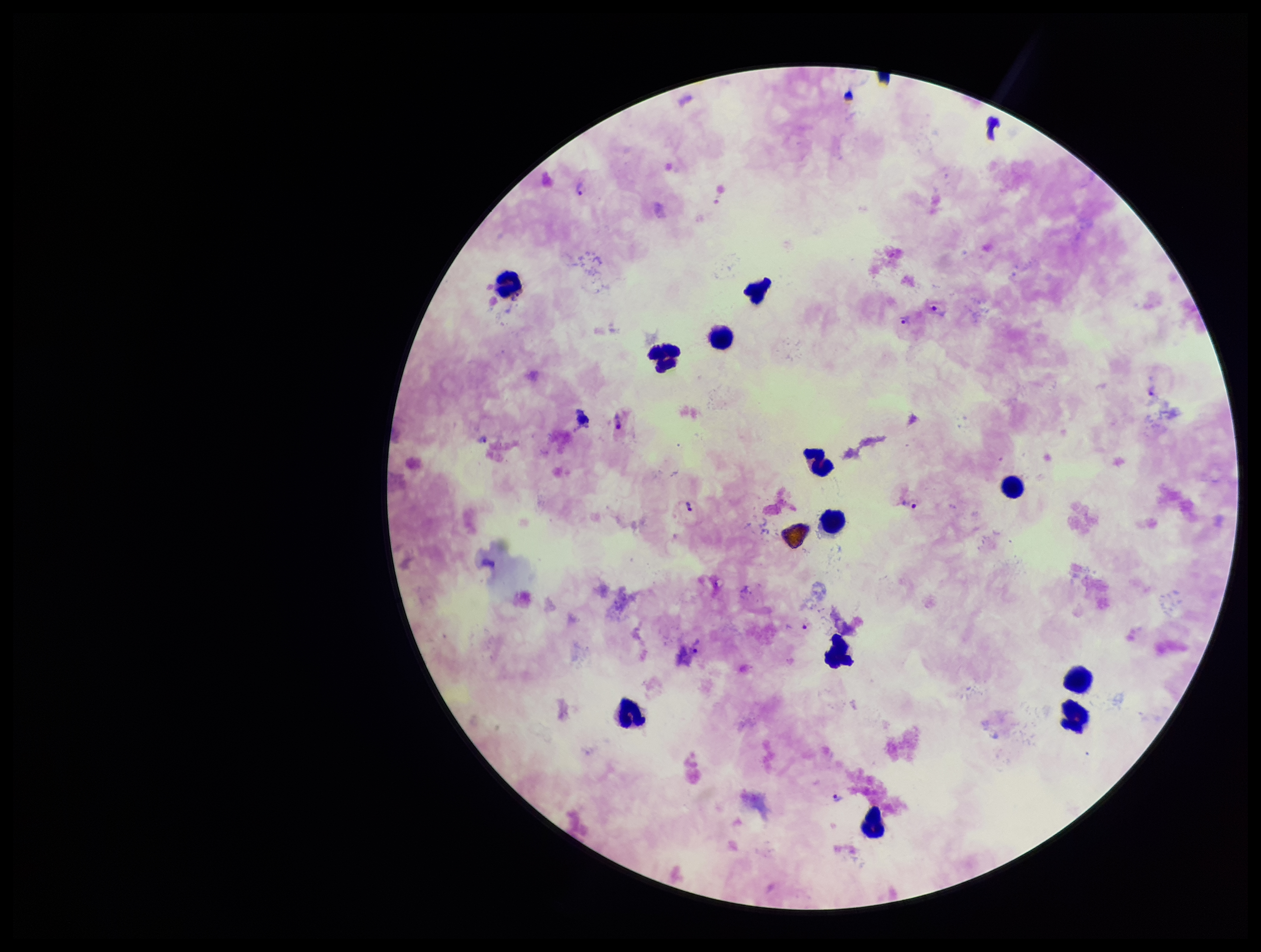

Summary:
  - Species reported for this patient: Plasmodium vivax
  - Field of view: single
  - Patient malaria status: positive
  - Stain: Giemsa
  - Plasmodium parasites: identified
  - Preparation: thick smear
  - Parasite count: 9
  - Image size: 1261×952 pixels
  - Capture: smartphone photograph through the microscope eyepiece
  - Leukocyte count: 12